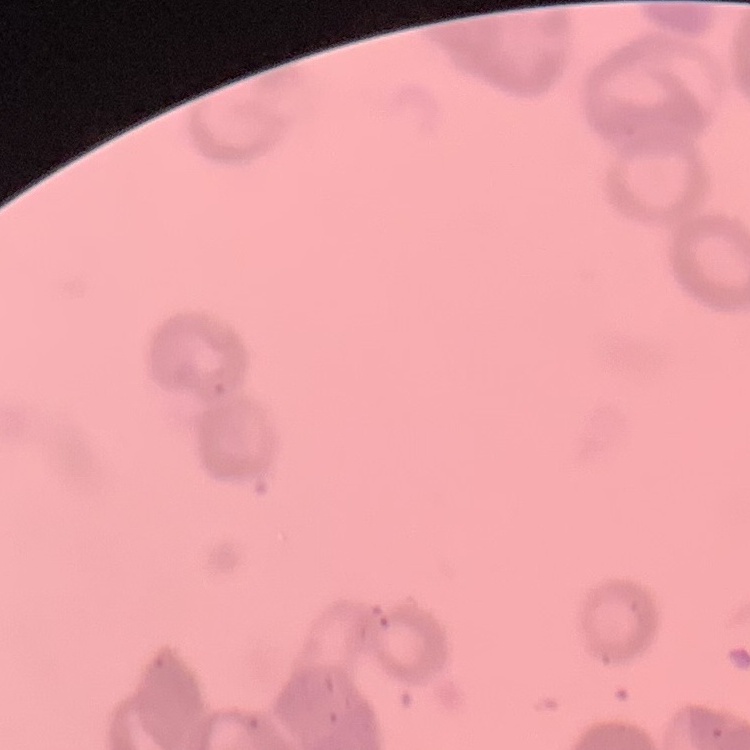
Summary:
  - Erythrocyte morphology: rouleaux formation
  - Stain: Field's or Giemsa
  - Preparation: thin blood film
  - Image type: one tile cut from a larger photomicrograph